Locate every blood parasite and identify its species.
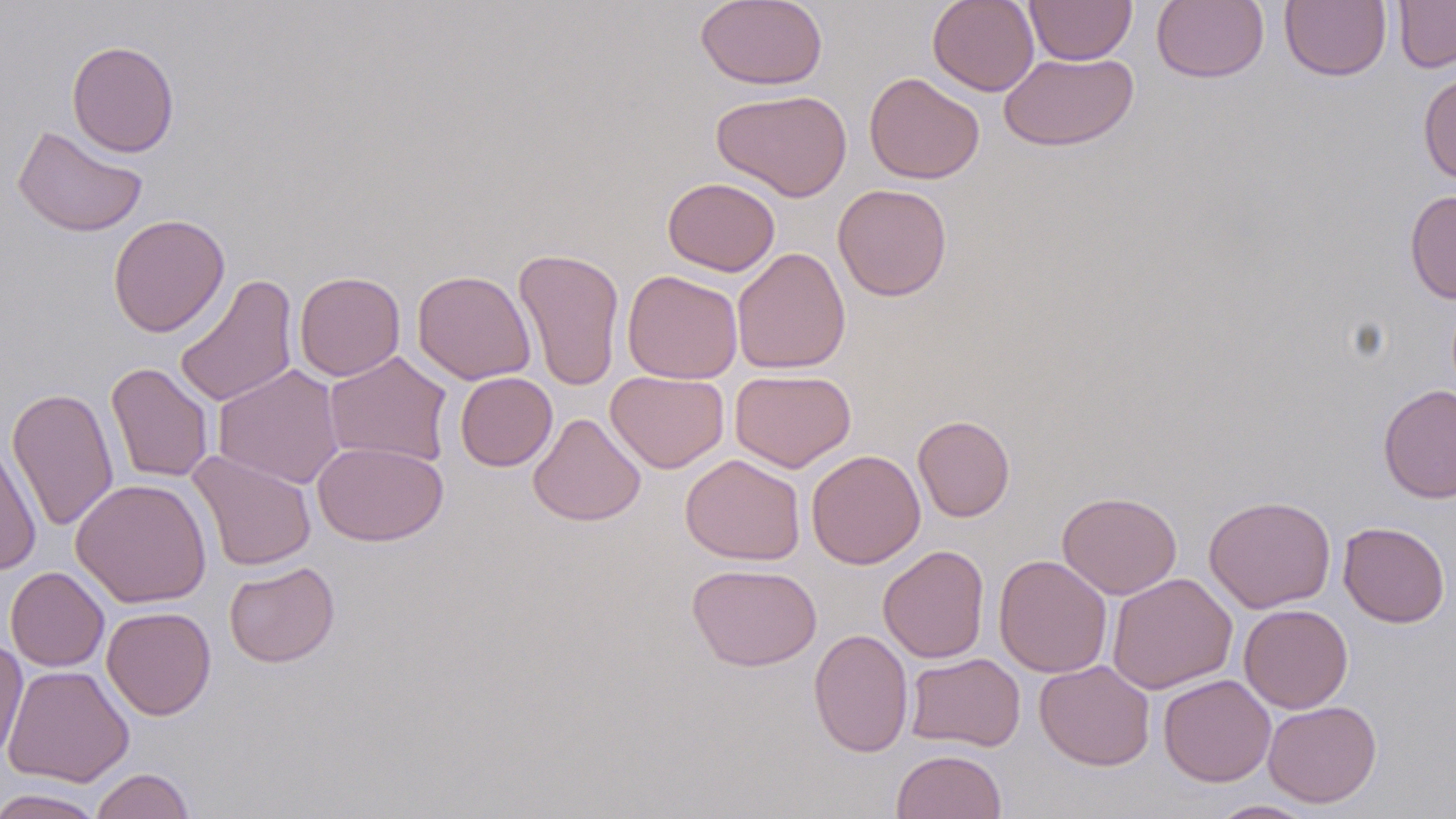
No blood parasites seen.

Approximate bounding boxes as named x1/y1/x2/y2 corners in pixels. Uninfected red blood cell locations: (x1=695, y1=0, x2=828, y2=90), (x1=927, y1=0, x2=1040, y2=96), (x1=1024, y1=0, x2=1137, y2=65), (x1=1152, y1=0, x2=1268, y2=83), (x1=1280, y1=0, x2=1391, y2=82), (x1=1392, y1=0, x2=1456, y2=73), (x1=66, y1=41, x2=179, y2=158), (x1=999, y1=52, x2=1139, y2=151), (x1=1418, y1=70, x2=1456, y2=185), (x1=864, y1=72, x2=985, y2=184), (x1=711, y1=89, x2=852, y2=202), (x1=12, y1=124, x2=148, y2=237), (x1=663, y1=177, x2=780, y2=276), (x1=833, y1=183, x2=952, y2=301), (x1=1405, y1=189, x2=1456, y2=304), (x1=108, y1=213, x2=230, y2=337), (x1=512, y1=247, x2=626, y2=392), (x1=732, y1=247, x2=851, y2=374), (x1=411, y1=269, x2=536, y2=385), (x1=622, y1=269, x2=743, y2=383), (x1=294, y1=271, x2=406, y2=381), (x1=174, y1=273, x2=299, y2=408), (x1=324, y1=351, x2=453, y2=467), (x1=106, y1=362, x2=214, y2=483), (x1=213, y1=364, x2=345, y2=489), (x1=730, y1=369, x2=856, y2=472), (x1=606, y1=370, x2=729, y2=473), (x1=455, y1=372, x2=557, y2=472), (x1=1377, y1=383, x2=1456, y2=504), (x1=6, y1=387, x2=119, y2=532), (x1=528, y1=412, x2=646, y2=526), (x1=913, y1=415, x2=1015, y2=522), (x1=0, y1=440, x2=42, y2=577), (x1=312, y1=441, x2=448, y2=546), (x1=187, y1=450, x2=317, y2=570), (x1=806, y1=450, x2=926, y2=569), (x1=680, y1=453, x2=805, y2=566), (x1=71, y1=478, x2=212, y2=608), (x1=1057, y1=491, x2=1182, y2=599), (x1=1204, y1=495, x2=1336, y2=613), (x1=1338, y1=521, x2=1450, y2=627), (x1=878, y1=544, x2=990, y2=663), (x1=993, y1=555, x2=1112, y2=678), (x1=223, y1=561, x2=340, y2=668), (x1=687, y1=562, x2=822, y2=671), (x1=5, y1=566, x2=109, y2=672), (x1=1106, y1=573, x2=1238, y2=695), (x1=1239, y1=604, x2=1354, y2=713), (x1=101, y1=606, x2=216, y2=720), (x1=808, y1=628, x2=913, y2=758), (x1=0, y1=637, x2=28, y2=763), (x1=905, y1=652, x2=1026, y2=751), (x1=1034, y1=660, x2=1155, y2=771), (x1=3, y1=663, x2=135, y2=787), (x1=1158, y1=674, x2=1276, y2=786), (x1=1263, y1=699, x2=1382, y2=808), (x1=891, y1=750, x2=1007, y2=818), (x1=91, y1=768, x2=195, y2=819), (x1=0, y1=788, x2=106, y2=819), (x1=1208, y1=800, x2=1318, y2=818). Slide-level diagnosis: no evidence of blood parasites. 1000x magnification. Single field of view. May-Grünwald-Giemsa stain. Optical microscopy. Thin blood film. Image is 1456×819 pixels.